State the blood parasite species.
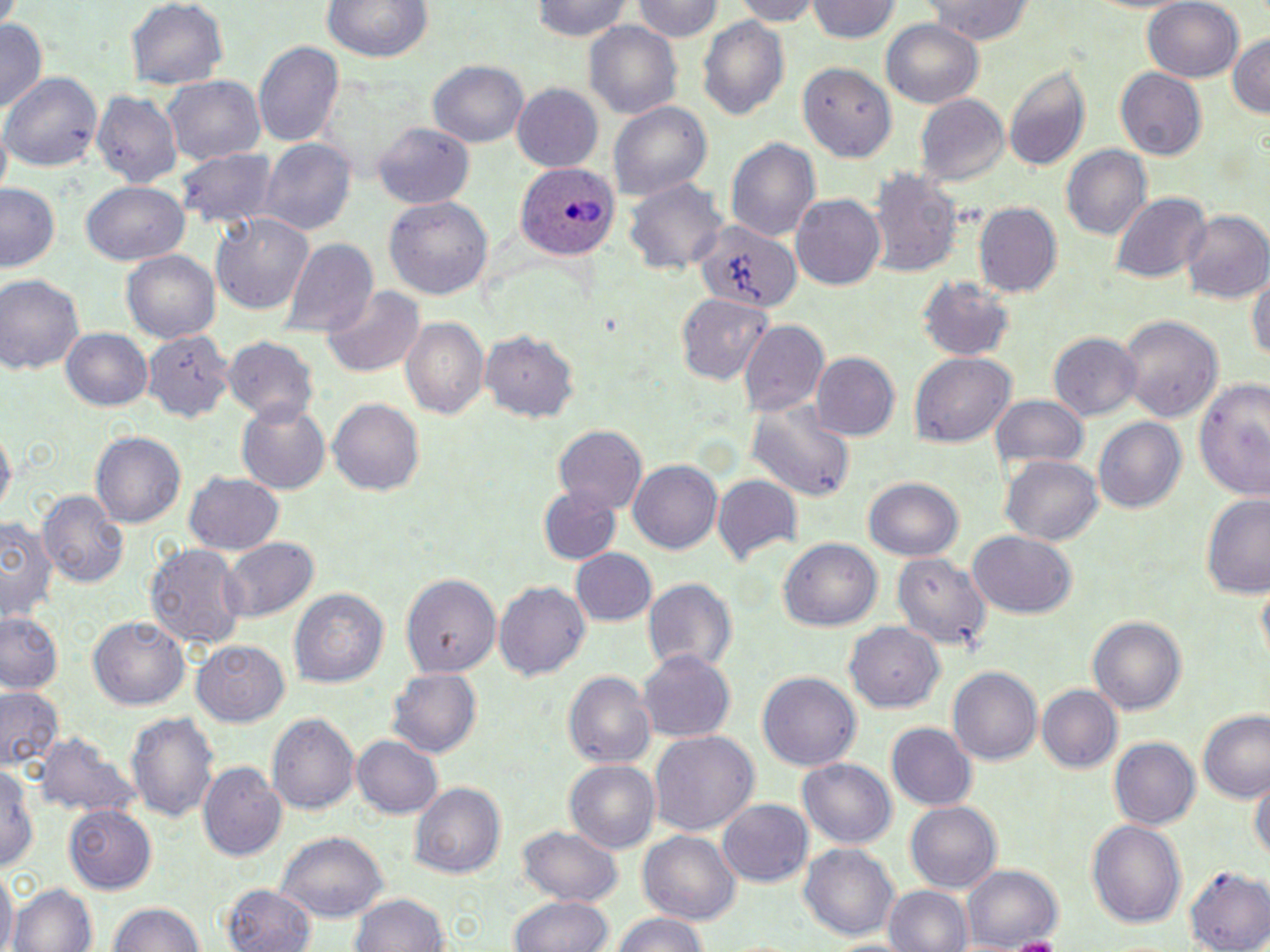

Plasmodium ovale.

Summary:
  - Coordinate format: approximate bounding boxes as (x1,y1)-(x2,y2) corner pairs in pixels
  - Plasmodium ovale-infected red blood cell locations: (516,163)-(618,261)
  - Uninfected red blood cell locations: (529,0)-(638,45), (630,0)-(723,44), (730,0)-(820,23), (806,0)-(900,44), (918,0)-(1037,45), (1143,0)-(1244,83), (318,1)-(437,63), (125,2)-(229,89), (696,15)-(791,125), (583,19)-(684,122), (880,20)-(985,108), (0,21)-(48,112), (1227,30)-(1270,122), (253,39)-(342,150), (430,62)-(528,150), (1004,64)-(1091,170), (802,66)-(896,163), (1115,69)-(1207,159), (4,72)-(101,176), (163,75)-(266,165), (514,83)-(603,171), (91,89)-(182,188), (913,95)-(1008,188), (607,100)-(712,202), (373,123)-(473,210), (725,137)-(821,245), (260,138)-(355,238), (1059,145)-(1151,242), (177,146)-(276,228), (868,169)-(963,277), (625,178)-(729,279), (81,180)-(189,267), (1,182)-(63,273), (1111,193)-(1210,284), (790,194)-(885,291), (385,196)-(492,297), (975,204)-(1062,298), (1182,212)-(1270,304), (210,214)-(314,318), (696,218)-(802,314), (281,239)-(378,339), (123,250)-(221,344), (1249,258)-(1269,375), (0,274)-(85,379), (917,279)-(1014,361), (320,284)-(424,377), (678,292)-(772,384), (1118,315)-(1223,425), (401,318)-(488,420), (737,322)-(830,417), (60,327)-(153,412), (1048,331)-(1142,419), (145,332)-(229,423), (479,332)-(578,425), (222,337)-(317,421), (909,352)-(1015,448), (811,353)-(900,438), (1195,375)-(1268,497), (991,394)-(1088,474), (327,397)-(424,496), (236,400)-(333,494), (746,401)-(854,503), (1095,418)-(1186,513), (552,424)-(649,514), (1,426)-(15,521), (91,431)-(184,527), (1000,455)-(1103,545), (628,459)-(721,555), (185,470)-(286,554), (711,475)-(803,566), (864,477)-(963,562), (538,484)-(621,565), (37,489)-(128,588), (1200,496)-(1270,599), (2,517)-(56,624), (968,531)-(1078,620), (221,537)-(317,623), (780,539)-(882,633), (145,542)-(248,651), (569,548)-(657,627), (893,550)-(992,651), (400,573)-(499,679), (643,576)-(737,678), (494,578)-(590,681), (289,586)-(389,690), (0,611)-(65,694), (1089,614)-(1185,717), (89,615)-(190,711), (842,623)-(945,713), (193,642)-(290,726), (638,652)-(737,743), (388,666)-(482,758), (946,666)-(1040,767), (564,672)-(655,769), (758,672)-(861,773), (1036,684)-(1122,773), (0,687)-(62,770), (266,711)-(360,814), (1197,712)-(1270,803), (128,713)-(218,825), (885,722)-(976,811), (37,732)-(137,819), (649,732)-(758,836), (351,737)-(441,817), (1108,737)-(1200,830), (0,757)-(39,877), (800,759)-(896,851), (564,760)-(659,855), (198,764)-(287,860), (1250,771)-(1268,871), (409,782)-(506,879), (719,799)-(812,886), (904,800)-(1004,893), (65,807)-(156,892), (1088,817)-(1185,925), (514,823)-(626,905), (638,830)-(740,924), (277,831)-(388,924), (799,844)-(899,941), (963,865)-(1061,949), (1186,868)-(1268,951), (0,870)-(15,952), (11,883)-(96,952), (222,885)-(319,952), (883,885)-(973,952), (348,890)-(452,952), (510,895)-(612,952), (107,900)-(208,952), (610,912)-(713,952)
  - Magnification: 1000x
  - Field of view: one of a larger specimen
  - Stain: May-Grünwald-Giemsa
  - Image size: 1270×952 pixels
  - Modality: optical microscopy
  - Preparation: thin blood film